Report the malaria status of this cell.
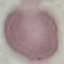
Uninfected.

Cell patch, automatically extracted from a larger field of view and resized to 64 × 64 pixels. Thin blood film. Giemsa-stained preparation. Photographed with a smartphone camera at the microscope eyepiece.